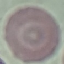

Summary:
  - Malaria status: uninfected
  - Preparation: thin blood film
  - Capture: smartphone camera at the microscope eyepiece
  - Stain: Giemsa
  - Image type: automatically extracted cell patch, resized to 64 × 64 pixels